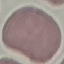

Summary:
  - Malaria status: uninfected
  - Stain: Giemsa
  - Image type: cell patch, automatically extracted from a larger field of view and resized to 64 × 64 pixels
  - Capture: smartphone through the microscope eyepiece
  - Preparation: thin smear